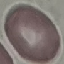
Result: no malaria parasites seen. Giemsa stain. Thin blood smear. Acquired by smartphone through the microscope eyepiece. Cell patch, automatically extracted from a larger field of view and resized to 64 × 64 pixels.